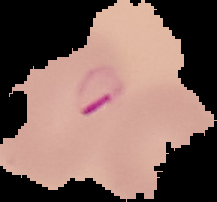
image type = segmented cell region on a black background
malaria status = parasitized
preparation = thin blood smear
image size = 217×202 pixels